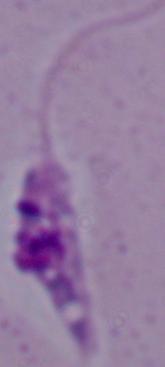
modality = photomicrograph
identification = Leishmania
magnification = 1000x